Assess this cell for malaria.
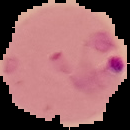
Parasitized.

image_type: segmented cell region on a black background
image_size: 130×130 pixels
preparation: thin blood smear